Classify this cell by malaria status.
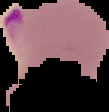
Parasitized.

From a thin blood film. Segmented cell region on a black background. Image is 109×112 pixels.